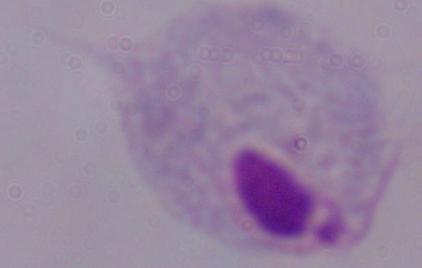
Summary:
  - Modality: micrograph
  - Magnification: 1000x
  - Identification: trichomonad